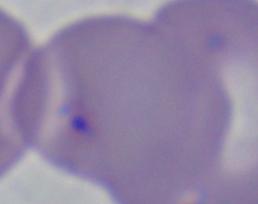

Summary:
  - Magnification: 1000x
  - Identification: Babesia
  - Modality: photomicrograph